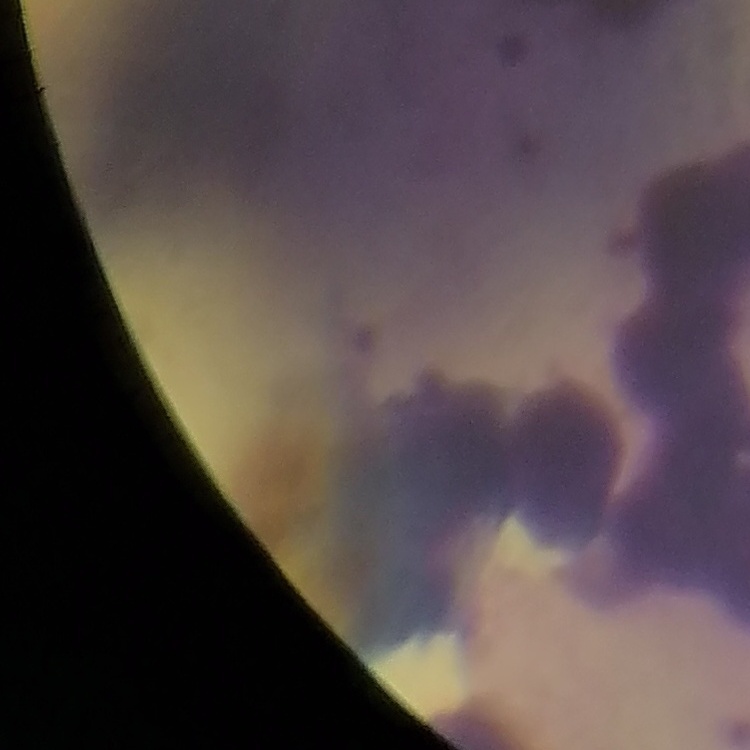

erythrocyte morphology = rouleaux formation
preparation = thin blood smear
stain = Field's or Giemsa
image type = square crop of a larger photomicrograph